Assess the morphology of the erythrocytes.
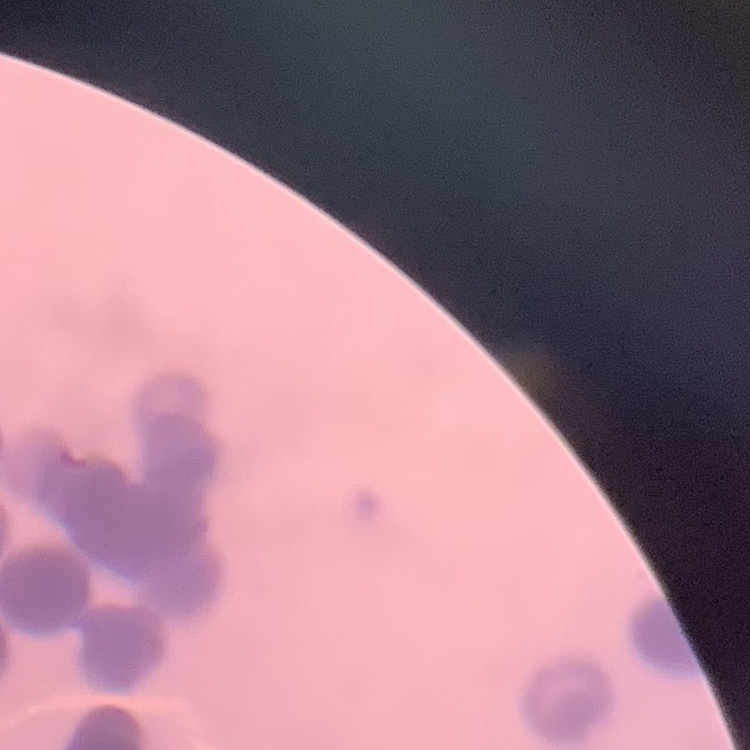

They show rouleaux formation.

Stained with either Field's or Giemsa. Square crop of a larger photomicrograph. Thin peripheral smear.